Outline each blood parasite and name the species.
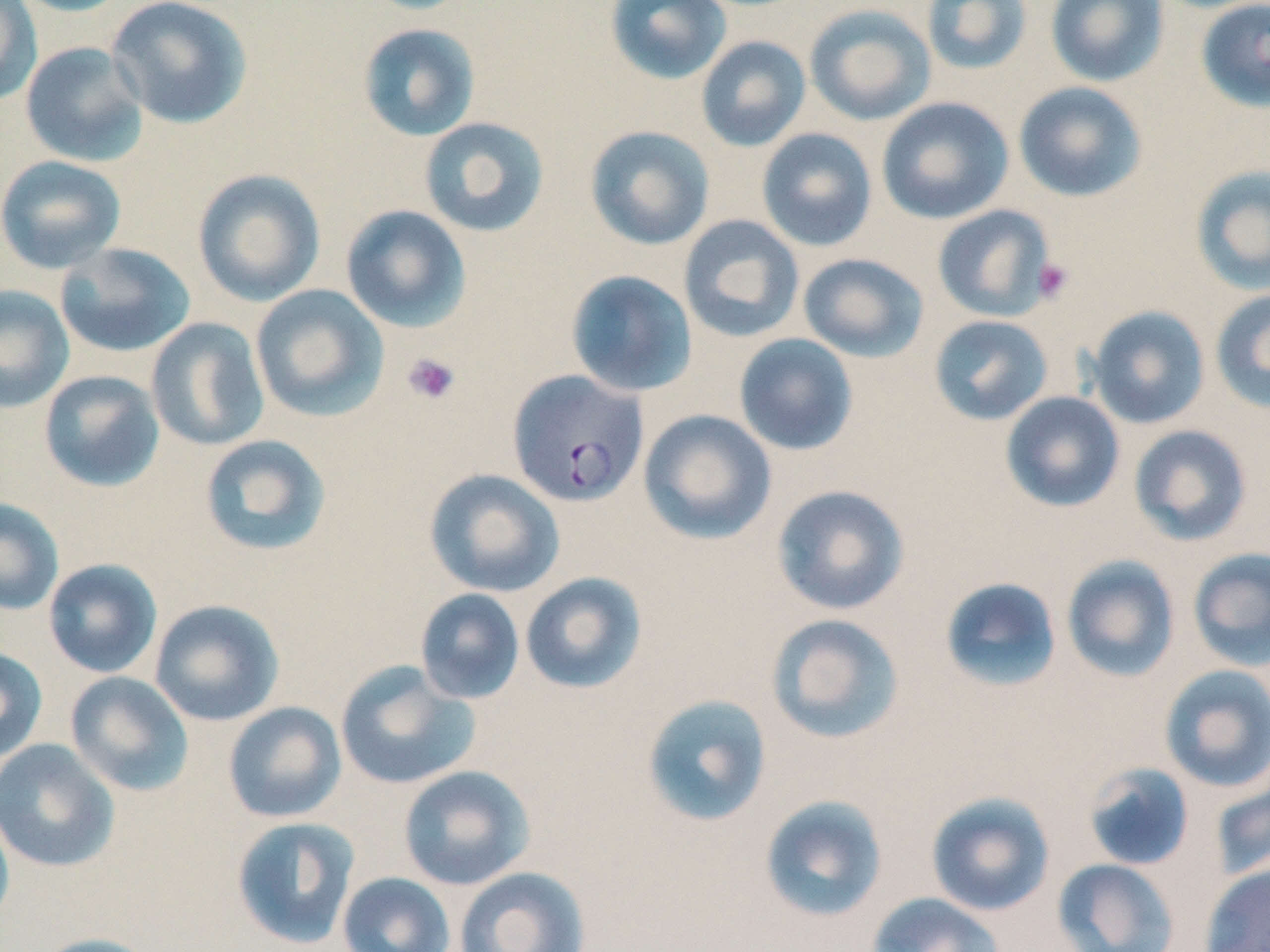

Approximate bounding boxes as named x1/y1/x2/y2 corners in pixels.
Plasmodium falciparum-infected red blood cells: (x1=507, y1=369, x2=648, y2=507).
No Plasmodium ovale, Plasmodium malariae, Plasmodium vivax, Babesia divergens, or Trypanosoma brucei observed.

Summary:
  - Platelet locations: (x1=1033, y1=257, x2=1074, y2=303), (x1=402, y1=353, x2=460, y2=405)
  - Uninfected red blood cell locations: (x1=0, y1=0, x2=42, y2=107), (x1=9, y1=0, x2=134, y2=17), (x1=106, y1=0, x2=254, y2=129), (x1=604, y1=0, x2=732, y2=85), (x1=921, y1=0, x2=1033, y2=76), (x1=1045, y1=0, x2=1170, y2=87), (x1=1195, y1=0, x2=1270, y2=113), (x1=804, y1=4, x2=936, y2=126), (x1=357, y1=23, x2=482, y2=142), (x1=695, y1=35, x2=812, y2=152), (x1=20, y1=41, x2=149, y2=168), (x1=1013, y1=81, x2=1148, y2=202), (x1=876, y1=97, x2=1014, y2=225), (x1=418, y1=117, x2=550, y2=238), (x1=584, y1=125, x2=715, y2=250), (x1=756, y1=128, x2=878, y2=252), (x1=0, y1=155, x2=127, y2=274), (x1=1190, y1=164, x2=1270, y2=295), (x1=192, y1=169, x2=326, y2=307), (x1=340, y1=204, x2=472, y2=333), (x1=932, y1=205, x2=1056, y2=322), (x1=678, y1=215, x2=804, y2=343), (x1=54, y1=242, x2=196, y2=358), (x1=797, y1=253, x2=929, y2=363), (x1=565, y1=269, x2=697, y2=397), (x1=0, y1=284, x2=75, y2=413), (x1=250, y1=284, x2=390, y2=423), (x1=1210, y1=289, x2=1270, y2=414), (x1=1085, y1=306, x2=1211, y2=429), (x1=928, y1=314, x2=1054, y2=426), (x1=146, y1=317, x2=270, y2=452), (x1=733, y1=333, x2=858, y2=456), (x1=38, y1=369, x2=165, y2=492), (x1=1000, y1=391, x2=1125, y2=513), (x1=638, y1=409, x2=777, y2=545), (x1=1128, y1=424, x2=1252, y2=546), (x1=199, y1=434, x2=332, y2=557), (x1=423, y1=468, x2=565, y2=598), (x1=771, y1=484, x2=910, y2=616), (x1=0, y1=497, x2=64, y2=616), (x1=1187, y1=547, x2=1270, y2=670), (x1=1061, y1=555, x2=1180, y2=683), (x1=43, y1=558, x2=163, y2=679), (x1=520, y1=571, x2=647, y2=694), (x1=939, y1=577, x2=1063, y2=694), (x1=414, y1=588, x2=526, y2=705), (x1=149, y1=599, x2=285, y2=726), (x1=765, y1=613, x2=906, y2=744), (x1=0, y1=646, x2=48, y2=764), (x1=335, y1=660, x2=481, y2=790), (x1=1158, y1=664, x2=1270, y2=794), (x1=64, y1=671, x2=195, y2=796), (x1=640, y1=693, x2=773, y2=828), (x1=222, y1=701, x2=347, y2=823), (x1=0, y1=738, x2=120, y2=873), (x1=1081, y1=762, x2=1195, y2=872), (x1=397, y1=765, x2=535, y2=891), (x1=1210, y1=777, x2=1270, y2=881), (x1=925, y1=791, x2=1056, y2=917), (x1=758, y1=794, x2=889, y2=923), (x1=0, y1=803, x2=15, y2=932), (x1=230, y1=816, x2=361, y2=950), (x1=1052, y1=858, x2=1182, y2=952), (x1=1199, y1=864, x2=1270, y2=952), (x1=453, y1=866, x2=591, y2=952), (x1=336, y1=872, x2=455, y2=952), (x1=867, y1=893, x2=1006, y2=952), (x1=32, y1=932, x2=161, y2=952)
  - Slide-level diagnosis: Plasmodium falciparum
  - Image size: 1270×952 pixels
  - Magnification: 1000x
  - Stain: May-Grünwald-Giemsa
  - Modality: optical microscopy
  - Preparation: thin blood film
  - Field of view: one of a larger specimen